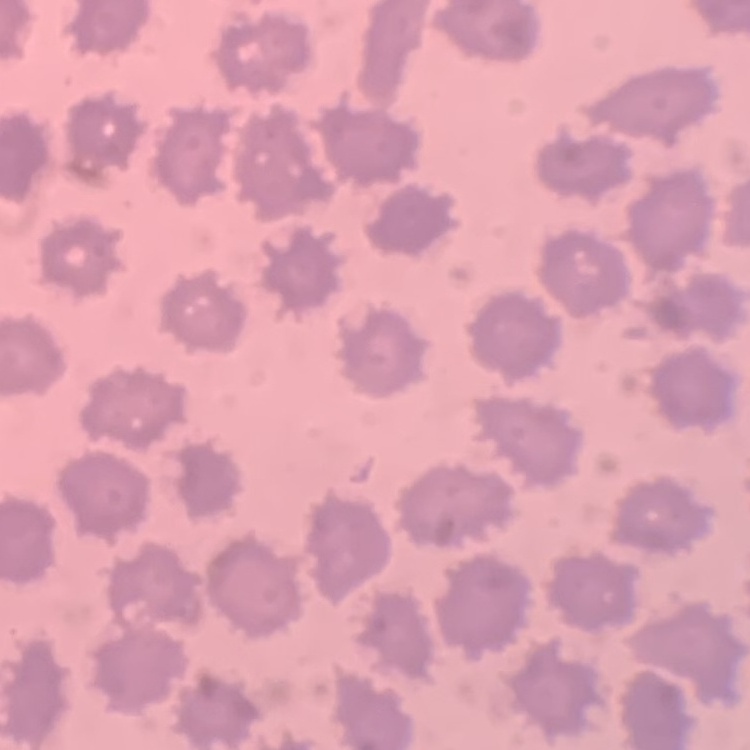 The red blood cells exhibit no rouleaux formation. Thin blood film. Field's or Giemsa stain. One tile cut from a larger photomicrograph.